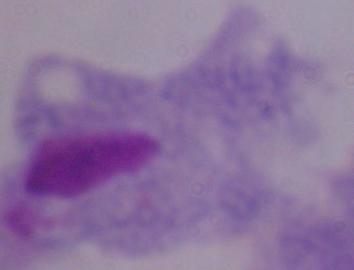
Summary:
  - Modality: micrograph
  - Magnification: 1000x
  - Identification: trichomonad